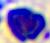
A white blood cell is seen. Photomicrograph. 400x magnification.